Identify the parasite.
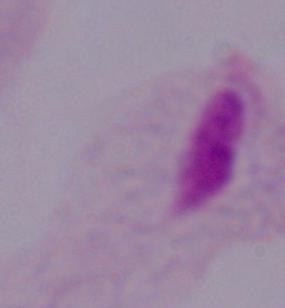

A trichomonad.

1000x magnification. Photomicrograph.